Identify the cell.
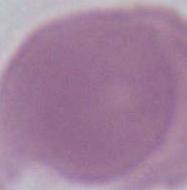

An erythrocyte.

modality = photomicrograph
magnification = 1000x